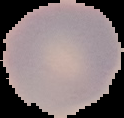 From a thin blood film. The area outside the segmented cell region is set to black. Image is 124×118 pixels. Result: no malaria parasites detected.